Name the cell type shown.
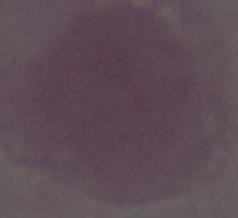
An erythrocyte.

modality = micrograph
magnification = 1000x